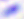

magnification = 400x
identification = Toxoplasma gondii
modality = photomicrograph